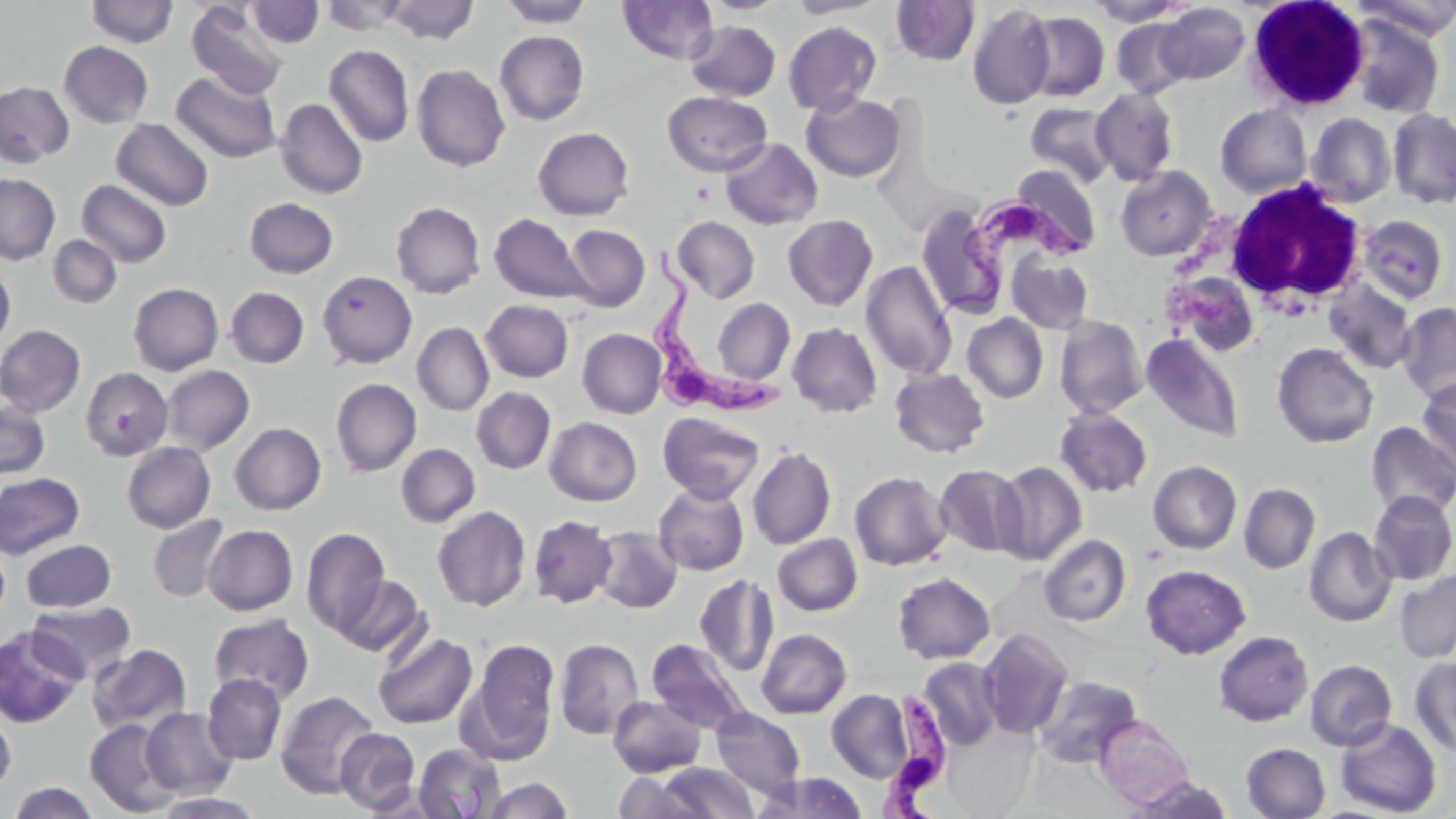

slide-level diagnosis = Trypanosoma brucei
field of view = single
modality = light microscopy
stain = May-Grünwald-Giemsa
platelet locations = approximate bounding boxes as named x1/y1/x2/y2 corners in pixels: (x1=692, y1=182, x2=716, y2=205)
white blood cell locations = approximate bounding boxes as named x1/y1/x2/y2 corners in pixels: (x1=1247, y1=0, x2=1374, y2=105), (x1=1223, y1=178, x2=1367, y2=315)
uninfected red blood cell locations = approximate bounding boxes as named x1/y1/x2/y2 corners in pixels: (x1=86, y1=0, x2=178, y2=47), (x1=319, y1=0, x2=412, y2=35), (x1=498, y1=0, x2=596, y2=27), (x1=617, y1=0, x2=718, y2=64), (x1=699, y1=0, x2=790, y2=16), (x1=787, y1=0, x2=886, y2=18), (x1=1084, y1=0, x2=1190, y2=26), (x1=1353, y1=0, x2=1456, y2=41), (x1=246, y1=1, x2=324, y2=47), (x1=383, y1=1, x2=479, y2=44), (x1=890, y1=1, x2=980, y2=66), (x1=186, y1=2, x2=289, y2=101), (x1=967, y1=3, x2=1056, y2=109), (x1=1157, y1=3, x2=1250, y2=84), (x1=1022, y1=11, x2=1110, y2=102), (x1=1347, y1=14, x2=1445, y2=119), (x1=1111, y1=18, x2=1195, y2=99), (x1=686, y1=20, x2=781, y2=102), (x1=783, y1=21, x2=882, y2=116), (x1=494, y1=30, x2=590, y2=125), (x1=58, y1=41, x2=153, y2=128), (x1=323, y1=44, x2=414, y2=147), (x1=412, y1=64, x2=510, y2=172), (x1=171, y1=71, x2=282, y2=164), (x1=0, y1=81, x2=74, y2=167), (x1=1090, y1=88, x2=1179, y2=185), (x1=662, y1=91, x2=772, y2=176), (x1=801, y1=92, x2=906, y2=182), (x1=275, y1=98, x2=368, y2=199), (x1=1026, y1=102, x2=1116, y2=187), (x1=1215, y1=104, x2=1312, y2=198), (x1=1388, y1=107, x2=1456, y2=209), (x1=1306, y1=113, x2=1396, y2=207), (x1=111, y1=118, x2=214, y2=211), (x1=532, y1=127, x2=634, y2=220), (x1=720, y1=138, x2=823, y2=230), (x1=1009, y1=164, x2=1102, y2=258), (x1=1115, y1=165, x2=1216, y2=261), (x1=0, y1=174, x2=60, y2=264), (x1=76, y1=179, x2=172, y2=268), (x1=245, y1=197, x2=338, y2=278), (x1=391, y1=201, x2=486, y2=299), (x1=915, y1=201, x2=1007, y2=321), (x1=490, y1=213, x2=591, y2=305), (x1=1357, y1=214, x2=1449, y2=304), (x1=673, y1=215, x2=760, y2=303), (x1=783, y1=215, x2=878, y2=311), (x1=563, y1=225, x2=649, y2=311), (x1=48, y1=235, x2=122, y2=308), (x1=1006, y1=252, x2=1094, y2=333), (x1=860, y1=260, x2=958, y2=380), (x1=0, y1=263, x2=15, y2=348), (x1=318, y1=271, x2=417, y2=368), (x1=1185, y1=273, x2=1256, y2=359), (x1=1324, y1=279, x2=1418, y2=375), (x1=128, y1=283, x2=223, y2=375), (x1=225, y1=287, x2=309, y2=368), (x1=711, y1=298, x2=794, y2=386), (x1=478, y1=299, x2=567, y2=474), (x1=480, y1=299, x2=574, y2=382), (x1=1396, y1=301, x2=1456, y2=405), (x1=962, y1=313, x2=1048, y2=404), (x1=1055, y1=315, x2=1148, y2=418), (x1=412, y1=322, x2=494, y2=415), (x1=787, y1=323, x2=882, y2=418), (x1=0, y1=325, x2=86, y2=416), (x1=578, y1=328, x2=666, y2=418), (x1=1142, y1=333, x2=1244, y2=443), (x1=1272, y1=342, x2=1378, y2=449), (x1=161, y1=365, x2=255, y2=455), (x1=80, y1=367, x2=172, y2=461), (x1=890, y1=368, x2=989, y2=457), (x1=1416, y1=377, x2=1456, y2=475), (x1=331, y1=378, x2=421, y2=477), (x1=471, y1=387, x2=556, y2=474), (x1=0, y1=400, x2=50, y2=479), (x1=1054, y1=408, x2=1153, y2=498), (x1=658, y1=412, x2=765, y2=504), (x1=545, y1=417, x2=642, y2=505), (x1=1366, y1=421, x2=1456, y2=519), (x1=230, y1=423, x2=326, y2=515), (x1=122, y1=442, x2=215, y2=533), (x1=396, y1=443, x2=480, y2=527), (x1=747, y1=446, x2=836, y2=550), (x1=1148, y1=460, x2=1242, y2=553), (x1=993, y1=461, x2=1087, y2=565), (x1=933, y1=464, x2=1028, y2=557), (x1=849, y1=470, x2=952, y2=571), (x1=0, y1=472, x2=85, y2=559), (x1=653, y1=482, x2=749, y2=575), (x1=1239, y1=483, x2=1320, y2=574), (x1=1368, y1=491, x2=1456, y2=585), (x1=432, y1=505, x2=531, y2=612), (x1=148, y1=514, x2=230, y2=603), (x1=528, y1=514, x2=618, y2=608), (x1=203, y1=524, x2=298, y2=615), (x1=301, y1=527, x2=389, y2=637), (x1=592, y1=527, x2=683, y2=614), (x1=1304, y1=527, x2=1396, y2=627), (x1=773, y1=534, x2=862, y2=615), (x1=1040, y1=534, x2=1131, y2=626), (x1=20, y1=539, x2=116, y2=612), (x1=0, y1=542, x2=9, y2=626), (x1=1141, y1=564, x2=1251, y2=658), (x1=1395, y1=569, x2=1456, y2=663), (x1=892, y1=572, x2=995, y2=664), (x1=335, y1=574, x2=430, y2=658), (x1=695, y1=574, x2=779, y2=678), (x1=30, y1=600, x2=136, y2=681), (x1=208, y1=614, x2=314, y2=705), (x1=1, y1=624, x2=88, y2=727), (x1=756, y1=628, x2=852, y2=719), (x1=977, y1=628, x2=1074, y2=740), (x1=1213, y1=630, x2=1313, y2=727), (x1=373, y1=631, x2=478, y2=729), (x1=463, y1=638, x2=560, y2=762), (x1=554, y1=638, x2=644, y2=740), (x1=647, y1=639, x2=752, y2=735), (x1=87, y1=644, x2=192, y2=736), (x1=1411, y1=656, x2=1456, y2=758), (x1=918, y1=657, x2=1003, y2=751), (x1=1305, y1=659, x2=1397, y2=751), (x1=202, y1=673, x2=287, y2=765), (x1=1033, y1=676, x2=1143, y2=769), (x1=275, y1=690, x2=381, y2=800), (x1=827, y1=690, x2=914, y2=782), (x1=608, y1=695, x2=707, y2=777), (x1=141, y1=708, x2=238, y2=798), (x1=711, y1=709, x2=806, y2=798), (x1=0, y1=711, x2=16, y2=795), (x1=1096, y1=716, x2=1194, y2=809), (x1=1334, y1=718, x2=1442, y2=817), (x1=84, y1=719, x2=182, y2=816), (x1=335, y1=728, x2=421, y2=813), (x1=413, y1=743, x2=507, y2=818), (x1=1241, y1=743, x2=1330, y2=819), (x1=657, y1=762, x2=760, y2=817), (x1=613, y1=772, x2=701, y2=819), (x1=753, y1=772, x2=869, y2=819), (x1=1126, y1=776, x2=1233, y2=818), (x1=483, y1=777, x2=572, y2=818), (x1=8, y1=782, x2=100, y2=818), (x1=154, y1=792, x2=266, y2=818)
image size = 1456×819 pixels
Trypanosoma brucei locations = approximate bounding boxes as named x1/y1/x2/y2 corners in pixels: (x1=933, y1=194, x2=1091, y2=344), (x1=643, y1=242, x2=783, y2=420), (x1=875, y1=688, x2=952, y2=819)
preparation = thin blood film
magnification = 1000x